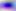

modality = photomicrograph
magnification = 400x
identification = Toxoplasma gondii